Locate and identify every blood parasite.
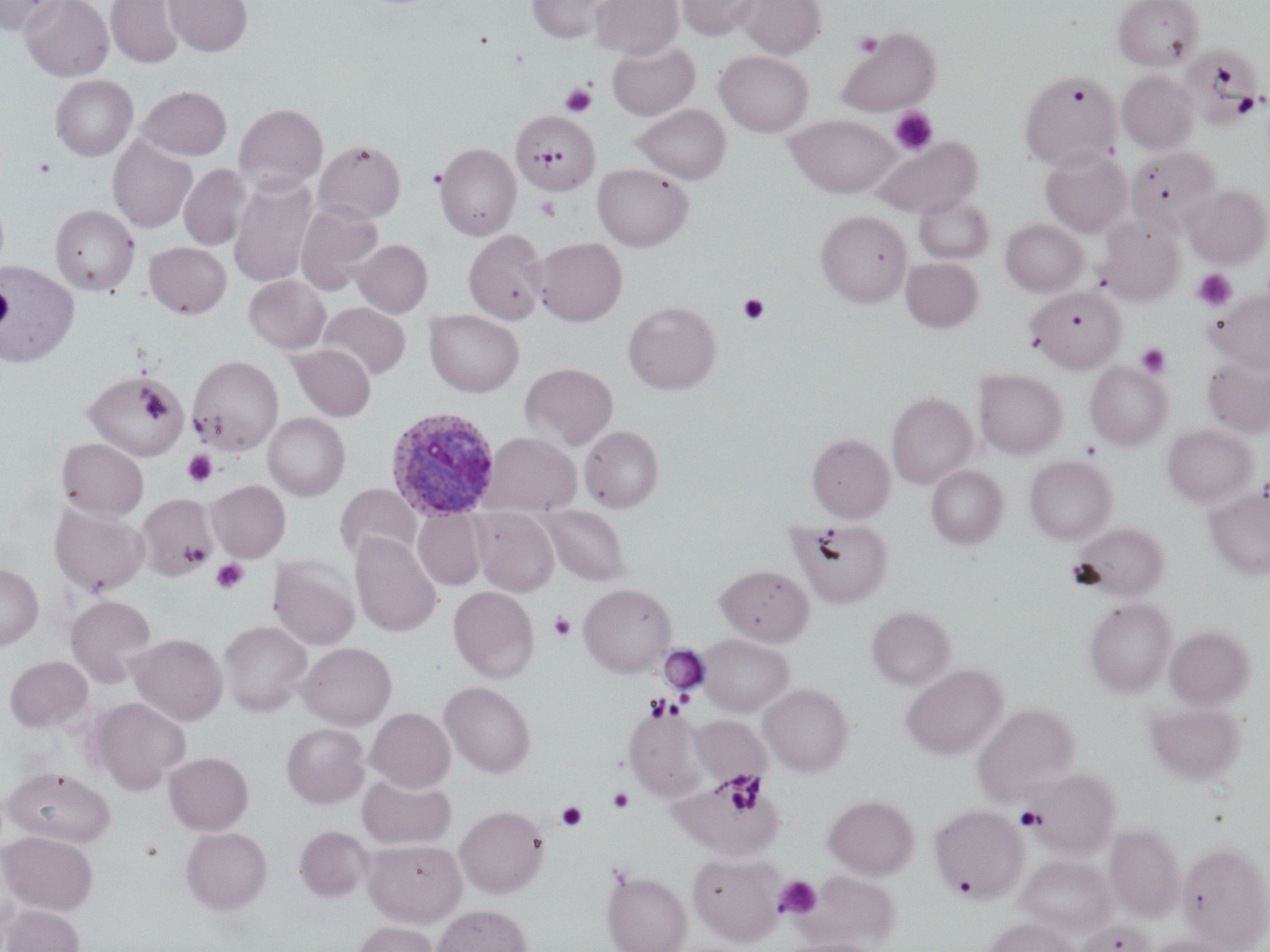

Approximate bounding boxes as (x1,y1)-(x2,y2) corner pairs in pixels.
Plasmodium ovale-infected red blood cells: (385,408)-(501,522).
No Plasmodium falciparum, Plasmodium malariae, Plasmodium vivax, Babesia divergens, or Trypanosoma brucei observed.

Summary:
  - Uninfected red blood cell locations: (0,0)-(67,36), (20,0)-(113,81), (164,0)-(252,56), (591,0)-(682,59), (677,0)-(758,40), (738,0)-(825,58), (1112,0)-(1203,70), (106,1)-(184,67), (527,1)-(611,43), (836,28)-(941,116), (607,41)-(699,120), (1191,43)-(1262,131), (715,50)-(813,137), (1117,70)-(1199,153), (1017,72)-(1118,171), (50,75)-(137,161), (139,86)-(231,160), (235,103)-(328,194), (633,104)-(731,183), (511,109)-(600,196), (784,114)-(901,198), (108,136)-(197,232), (871,136)-(981,218), (314,140)-(406,223), (435,143)-(521,240), (1127,146)-(1223,232), (1040,149)-(1132,237), (179,164)-(251,250), (592,164)-(693,251), (229,177)-(319,287), (1183,184)-(1269,266), (914,193)-(994,265), (295,203)-(383,294), (50,205)-(139,296), (816,210)-(912,306), (1096,216)-(1184,305), (1001,219)-(1088,296), (464,230)-(548,324), (533,237)-(627,326), (352,239)-(432,317), (145,242)-(231,318), (901,257)-(983,333), (0,261)-(80,368), (244,275)-(330,354), (1027,285)-(1125,372), (1208,289)-(1269,373), (623,301)-(721,395), (318,302)-(410,379), (424,309)-(524,397), (289,344)-(376,420), (190,355)-(284,453), (1202,357)-(1270,436), (520,362)-(618,450), (1085,362)-(1171,450), (974,369)-(1066,459), (83,370)-(188,460), (886,393)-(977,488), (264,413)-(349,500), (1163,424)-(1257,507), (579,426)-(664,512), (481,432)-(581,517), (807,433)-(894,522), (57,438)-(148,520), (1024,455)-(1116,544), (926,465)-(1008,548), (207,480)-(290,561), (336,484)-(421,564), (1204,488)-(1270,580), (136,494)-(217,580), (50,504)-(148,597), (541,505)-(630,585), (413,508)-(485,590), (471,508)-(558,596), (790,518)-(892,607), (1071,522)-(1170,600), (350,534)-(441,637), (269,556)-(360,650), (0,563)-(43,650), (716,564)-(813,646), (579,583)-(676,676), (448,586)-(539,683), (65,595)-(157,687), (1084,597)-(1176,697), (867,606)-(955,690), (218,620)-(311,716), (1165,625)-(1254,709), (128,633)-(228,725), (697,634)-(794,716), (298,642)-(396,730), (4,656)-(93,732), (901,664)-(1007,760), (440,681)-(536,778), (758,683)-(854,777), (89,697)-(190,794), (1145,701)-(1245,786), (973,702)-(1080,801), (623,705)-(706,801), (366,707)-(455,792), (691,716)-(771,786), (282,723)-(369,808), (164,752)-(253,835), (3,767)-(115,847), (1025,767)-(1120,857), (673,771)-(785,858), (358,772)-(456,849), (823,793)-(919,879), (931,804)-(1028,902), (455,805)-(550,898), (1105,822)-(1185,920), (295,826)-(372,902), (1108,826)-(1264,935), (181,827)-(272,914), (1,831)-(98,916), (363,839)-(466,925), (1179,841)-(1269,950), (689,853)-(785,945), (1016,855)-(1115,939), (601,869)-(691,952), (802,870)-(901,949), (2,904)-(84,952), (430,904)-(532,952), (984,918)-(1081,952), (1077,919)-(1155,952), (354,921)-(439,952), (1142,935)-(1231,952), (781,937)-(882,952)
  - Platelet locations: (854,32)-(883,57), (560,83)-(596,117), (889,106)-(938,156), (34,158)-(56,178), (1193,268)-(1237,312), (0,282)-(13,332), (738,294)-(769,325), (1136,343)-(1171,379), (140,390)-(171,420), (190,411)-(214,440), (183,450)-(217,487), (183,539)-(212,566), (211,558)-(248,594), (549,611)-(576,641), (659,647)-(709,695), (646,695)-(675,722), (720,771)-(764,813), (607,787)-(635,813), (556,801)-(588,831), (1016,807)-(1045,831), (952,874)-(977,899), (774,875)-(822,919)
  - Slide-level diagnosis: Plasmodium ovale
  - Magnification: 1000x
  - Stain: May-Grünwald-Giemsa
  - Preparation: thin blood film
  - Field of view: one of a larger specimen
  - Image size: 1270×952 pixels
  - Modality: light microscopy